Report the malaria status of this cell.
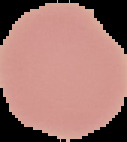
It is uninfected.

From a thin blood film. Cell region segmented out of the field of view; the surrounding area is masked to black. Image is 127×142 pixels.